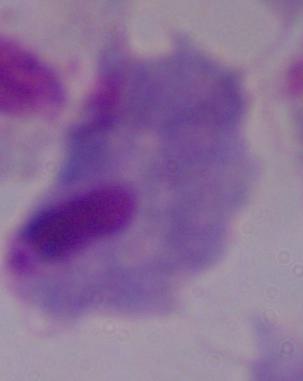 Captured at 1000x magnification. A trichomonad is seen. Micrograph.